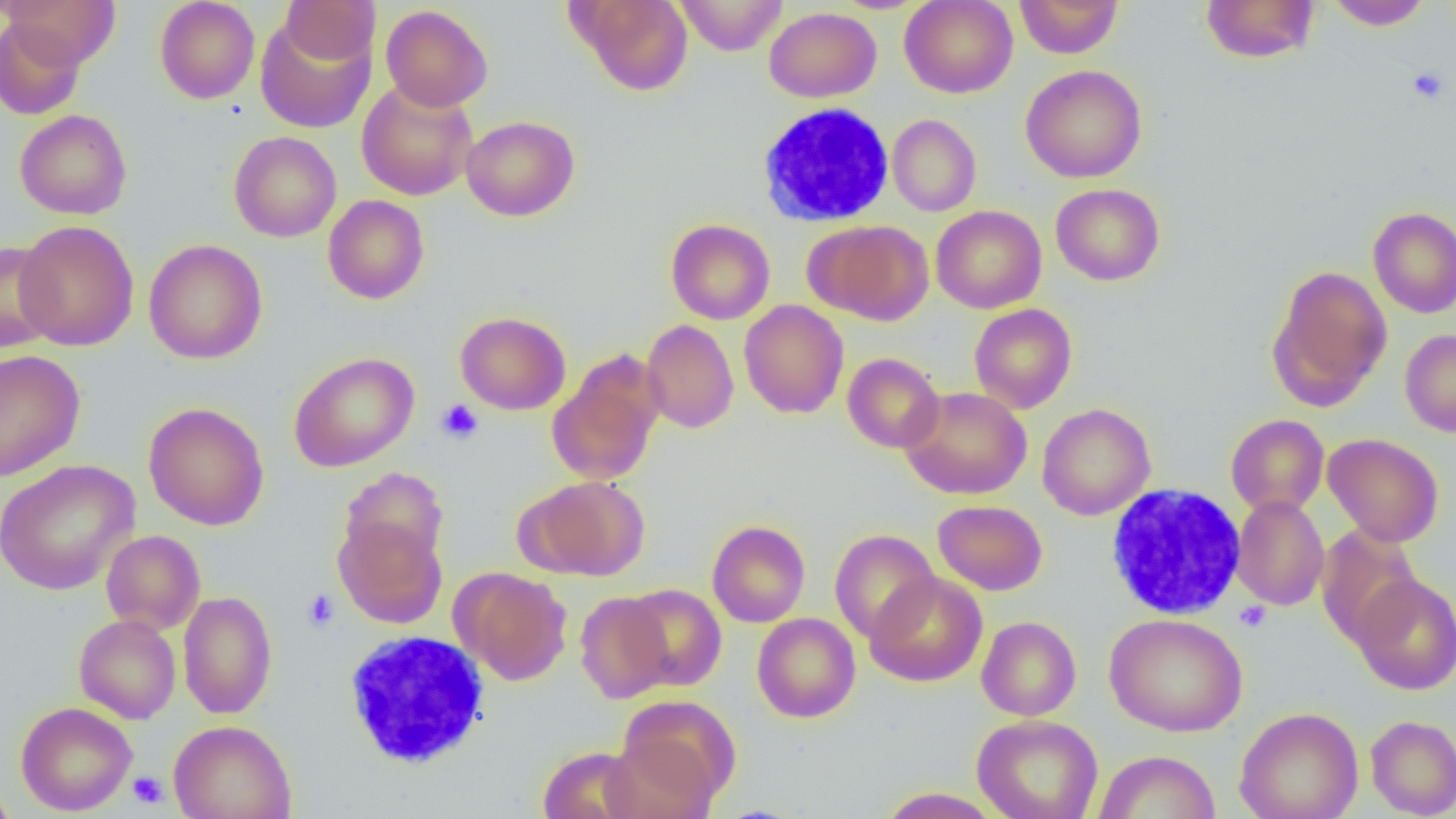

Summary:
  - Coordinate format: approximate bounding boxes as (x1, y1, x2, y2) in pixels
  - White blood cell locations (subset): (1105, 483, 1248, 620), (343, 629, 492, 770)
  - Uninfected red blood cell locations (subset): (4, 0, 121, 69), (155, 0, 260, 104), (280, 0, 380, 64), (570, 0, 693, 96), (675, 0, 788, 55), (899, 0, 1018, 98), (1014, 0, 1124, 58), (1200, 1, 1320, 64), (1326, 1, 1432, 31), (380, 4, 493, 112), (764, 7, 882, 102), (255, 14, 377, 133), (0, 16, 85, 120), (1021, 64, 1147, 183), (356, 80, 478, 201), (15, 109, 132, 219), (887, 114, 981, 216), (461, 115, 580, 221), (229, 131, 342, 242), (1051, 183, 1164, 285), (323, 195, 430, 304), (931, 205, 1047, 313), (1368, 207, 1456, 318), (665, 219, 775, 324), (15, 220, 139, 351), (810, 220, 934, 325), (143, 239, 268, 364), (0, 240, 60, 353), (1268, 265, 1393, 409), (739, 300, 849, 419), (969, 303, 1077, 414), (454, 311, 571, 415), (641, 319, 739, 433), (1400, 329, 1456, 437), (0, 349, 85, 481), (289, 351, 419, 472), (842, 353, 945, 453), (546, 357, 664, 486), (900, 386, 1032, 500), (143, 401, 269, 530), (1037, 403, 1155, 521), (1225, 414, 1329, 517), (1322, 433, 1444, 546), (0, 458, 140, 596), (339, 467, 449, 572), (527, 475, 650, 580), (1231, 495, 1329, 610), (933, 500, 1047, 595), (334, 516, 447, 628), (707, 519, 810, 627), (1316, 526, 1423, 647), (830, 529, 939, 644), (101, 530, 205, 635), (456, 568, 572, 685), (865, 572, 988, 687), (1351, 572, 1456, 695), (622, 583, 727, 692), (178, 591, 277, 719), (575, 592, 674, 703), (752, 613, 861, 723), (1104, 613, 1248, 737), (74, 614, 181, 724), (976, 616, 1081, 721), (612, 695, 740, 809), (15, 702, 137, 816), (1234, 706, 1364, 819), (972, 714, 1103, 819), (1365, 714, 1456, 818), (169, 720, 296, 819), (537, 745, 644, 819), (1095, 750, 1221, 819), (0, 779, 17, 819), (876, 787, 1004, 818)
  - Platelet locations: (1407, 67, 1449, 104), (436, 398, 484, 444), (302, 589, 340, 632), (1234, 601, 1271, 632), (128, 771, 168, 808)
  - Slide-level diagnosis: negative for blood parasites
  - Magnification: 1000x
  - Modality: light microscopy
  - Preparation: thin blood film
  - Field of view: single
  - Image size: 1456×819 pixels